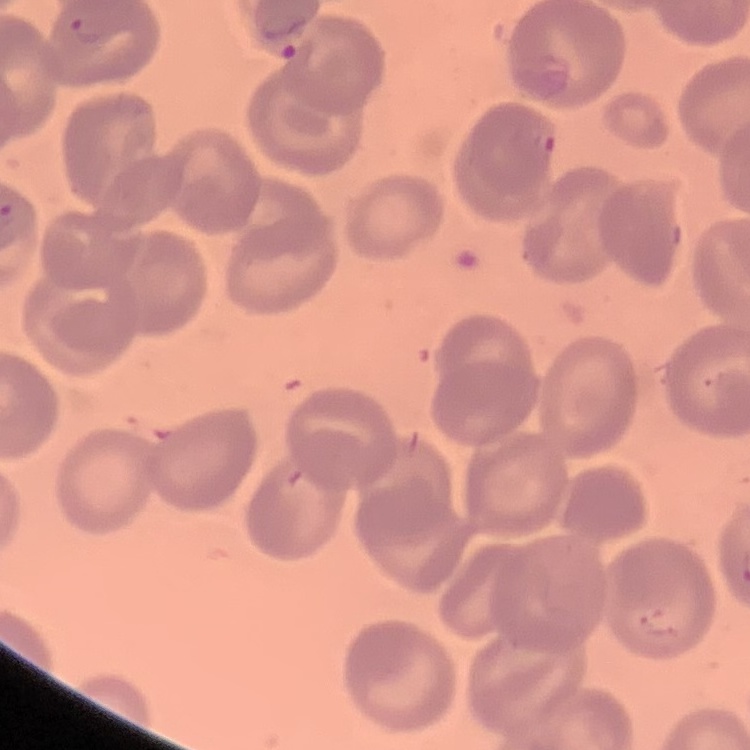
The erythrocytes exhibit no rouleaux formation. Square crop of a larger photomicrograph. Thin blood film. Stained with either Field's or Giemsa.